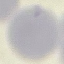

{
  "result": "no malaria parasites detected",
  "capture": "smartphone through the microscope eyepiece",
  "image_type": "cell patch, automatically extracted from a larger field of view and resized to 64 × 64 pixels",
  "stain": "Giemsa",
  "preparation": "thin blood smear"
}